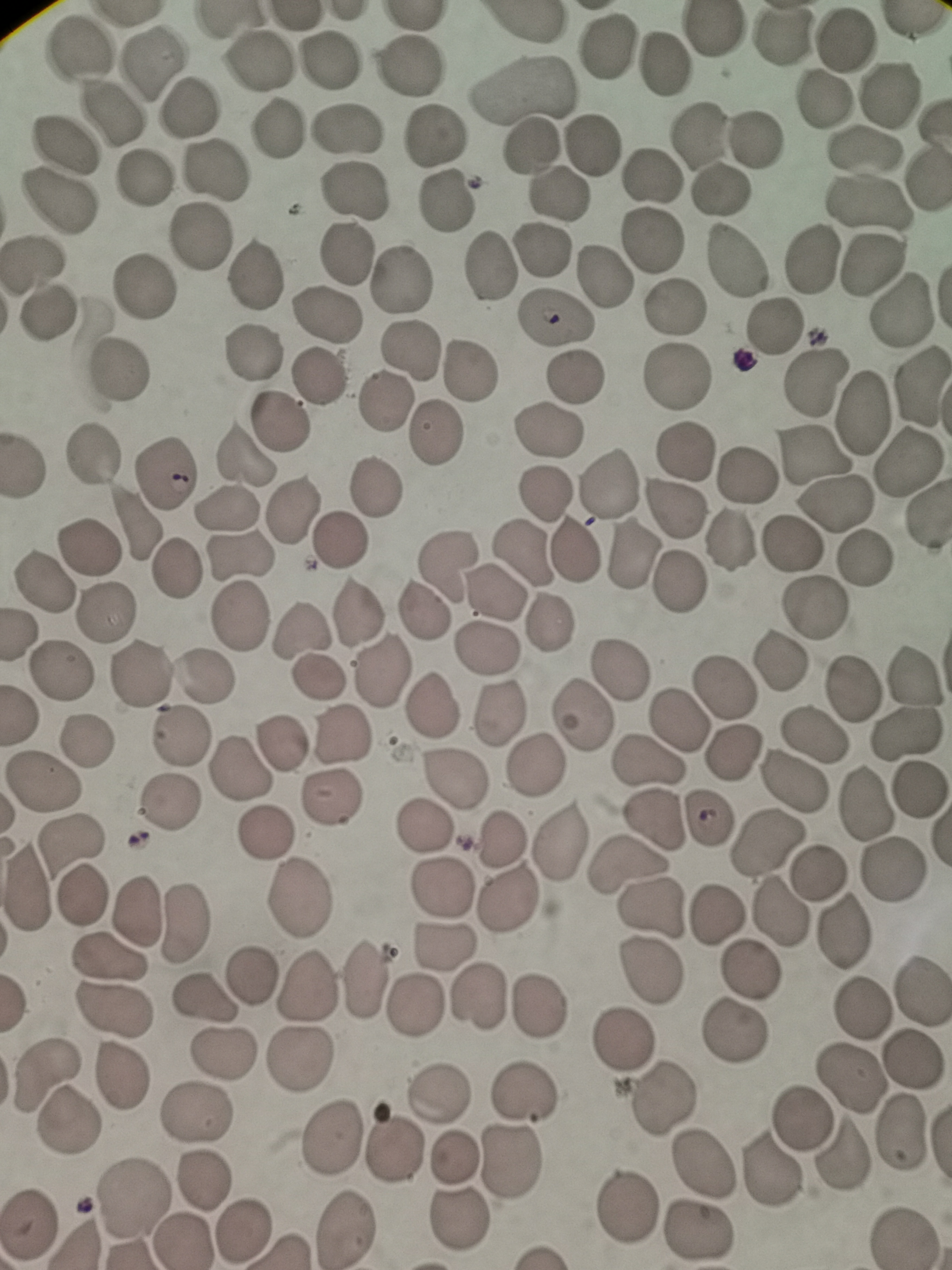 Approximate centers as (x, y) in pixels. Cell locations: (780, 37), (844, 40), (606, 43), (76, 49), (258, 59), (334, 61), (152, 63), (664, 67), (407, 69), (525, 90), (888, 95), (822, 99), (188, 109), (112, 112), (275, 128), (346, 131), (701, 133), (759, 137), (433, 138), (592, 144), (62, 145), (532, 146), (861, 151), (214, 168), (652, 176), (143, 181), (721, 190), (352, 194), (557, 197), (56, 203), (446, 203), (870, 204), (201, 236), (654, 242), (347, 256), (812, 257), (733, 260), (33, 263), (491, 268), (253, 276), (603, 276), (402, 278), (139, 287), (673, 305), (902, 309), (49, 313), (330, 314), (556, 320), (774, 325), (414, 349), (255, 351), (119, 371), (469, 371), (574, 377), (679, 377), (316, 378), (814, 378), (920, 388), (384, 401), (863, 409), (277, 419), (549, 429), (433, 433), (683, 450), (92, 455), (244, 456), (815, 457), (905, 458), (163, 474), (747, 474), (376, 485), (605, 488), (544, 491), (836, 504), (678, 508), (226, 509), (294, 511), (134, 520), (341, 541), (729, 541), (792, 542), (88, 548), (575, 550), (524, 551), (241, 555), (635, 556), (863, 558), (446, 563), (176, 571), (681, 582), (45, 583), (493, 592), (814, 606), (359, 610), (102, 611), (423, 611), (240, 614), (546, 623), (301, 631), (485, 649), (780, 663), (64, 671), (382, 671), (623, 672), (140, 675), (915, 676), (318, 677), (204, 678), (723, 686), (854, 686), (428, 708), (495, 714), (580, 718), (681, 719), (911, 734), (179, 735), (344, 737), (816, 737), (87, 739), (286, 740), (732, 752), (648, 762), (534, 765), (241, 771), (454, 778), (795, 781), (45, 784), (919, 792), (332, 797), (172, 805), (865, 805), (709, 816), (651, 820), (421, 826), (267, 834), (764, 838), (500, 839), (70, 841), (561, 841), (627, 867), (890, 871), (818, 872), (25, 885), (441, 888), (79, 896), (507, 899), (299, 900), (137, 908), (652, 908), (778, 910), (719, 916), (183, 924), (841, 934), (445, 945), (106, 958), (751, 970), (648, 971), (248, 976), (365, 981), (307, 984), (922, 995), (202, 996), (478, 999), (415, 1003), (541, 1007), (862, 1007), (110, 1014), (736, 1031), (625, 1039), (221, 1052), (298, 1061), (913, 1062), (44, 1074), (123, 1074), (850, 1079), (526, 1093), (441, 1095), (664, 1096), (195, 1114), (801, 1118), (68, 1122), (903, 1130), (332, 1137), (395, 1147), (842, 1156), (452, 1157), (516, 1158), (705, 1162), (771, 1172), (203, 1179), (135, 1196), (629, 1205), (458, 1220), (26, 1222), (343, 1225), (240, 1230), (697, 1232), (181, 1241). Acquired by smartphone through the microscope eyepiece. Image is 952×1270 pixels. One field from this slide. Giemsa stain. Thin blood smear.